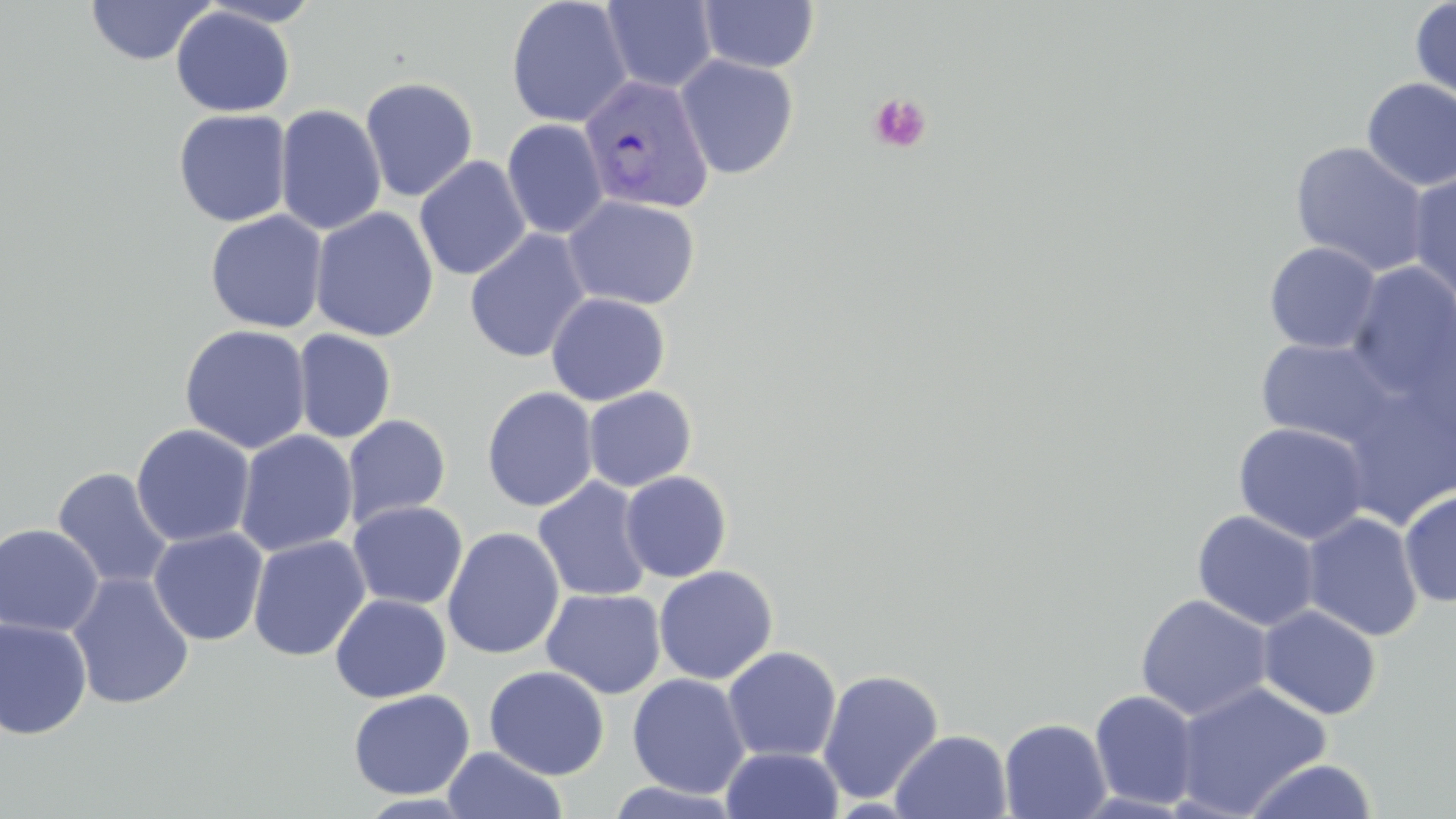

slide_level_diagnosis: Plasmodium vivax
stain: May-Grünwald-Giemsa
image_size: 1456×819 pixels
plasmodium_vivax_infected_red_blood_cell_locations: 'approximate bounding boxes as (x1, y1, x2, y2) in pixels: (578, 73, 715, 214)'
uninfected_red_blood_cell_locations: 'approximate bounding boxes as (x1, y1, x2, y2) in pixels: (84, 0, 216, 66), (506, 0, 632, 128), (697, 0, 819, 73), (1409, 0, 1456, 108), (601, 1, 718, 93), (170, 6, 296, 117), (675, 55, 799, 180), (359, 76, 479, 202), (1361, 78, 1456, 191), (274, 104, 387, 236), (173, 108, 292, 227), (502, 118, 608, 239), (1290, 141, 1430, 277), (414, 156, 531, 280), (1407, 172, 1456, 303), (562, 195, 701, 309), (309, 207, 439, 342), (204, 210, 328, 333), (465, 229, 591, 364), (1264, 242, 1382, 354), (1347, 263, 1456, 396), (545, 293, 670, 406), (179, 324, 311, 454), (292, 329, 397, 443), (1254, 336, 1397, 447), (583, 386, 697, 492), (481, 387, 599, 511), (342, 415, 452, 528), (1233, 422, 1370, 545), (131, 423, 256, 548), (234, 430, 358, 557), (52, 467, 174, 591), (620, 471, 733, 583), (533, 477, 653, 602), (1399, 490, 1456, 607), (348, 500, 468, 610), (1192, 510, 1320, 631), (1301, 511, 1424, 642), (0, 523, 104, 637), (148, 527, 268, 646), (442, 527, 565, 660), (248, 535, 371, 662), (654, 566, 778, 684), (66, 572, 194, 710), (541, 588, 666, 699), (329, 593, 451, 703), (1135, 594, 1273, 721), (1257, 605, 1382, 720), (0, 617, 93, 739), (722, 646, 842, 763), (484, 665, 609, 779), (817, 668, 944, 804), (627, 673, 750, 799), (1173, 681, 1331, 817), (348, 688, 476, 800), (1089, 689, 1200, 811), (999, 717, 1111, 819), (891, 729, 1013, 818), (442, 747, 568, 819), (721, 747, 843, 818), (1241, 758, 1379, 818), (604, 781, 745, 818)'
preparation: thin blood smear
field_of_view: one of a larger specimen
modality: light microscopy
magnification: 1000x
platelet_locations: 'approximate bounding boxes as (x1, y1, x2, y2) in pixels: (868, 92, 932, 154)'